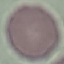

Summary:
  - Malaria status: uninfected
  - Image type: cell patch, automatically extracted from a larger field of view and resized to 64 × 64 pixels
  - Capture: smartphone camera at the microscope eyepiece
  - Stain: Giemsa
  - Preparation: thin blood smear